Report the malaria status of this cell.
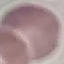
It is uninfected.

Summary:
  - Image type: automatically extracted cell patch, resized to 64 × 64 pixels
  - Preparation: thin blood film
  - Capture: smartphone camera at the microscope eyepiece
  - Stain: Giemsa